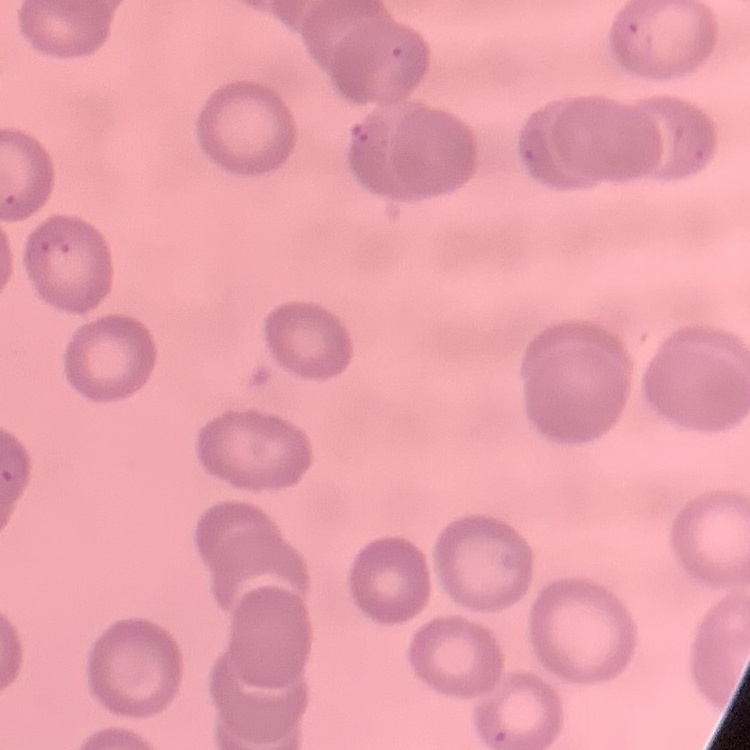
The red blood cells exhibit no rouleaux formation. Thin blood smear. Stained with either Field's or Giemsa. One tile cut from a larger photomicrograph.